Locate every Plasmodium parasite.
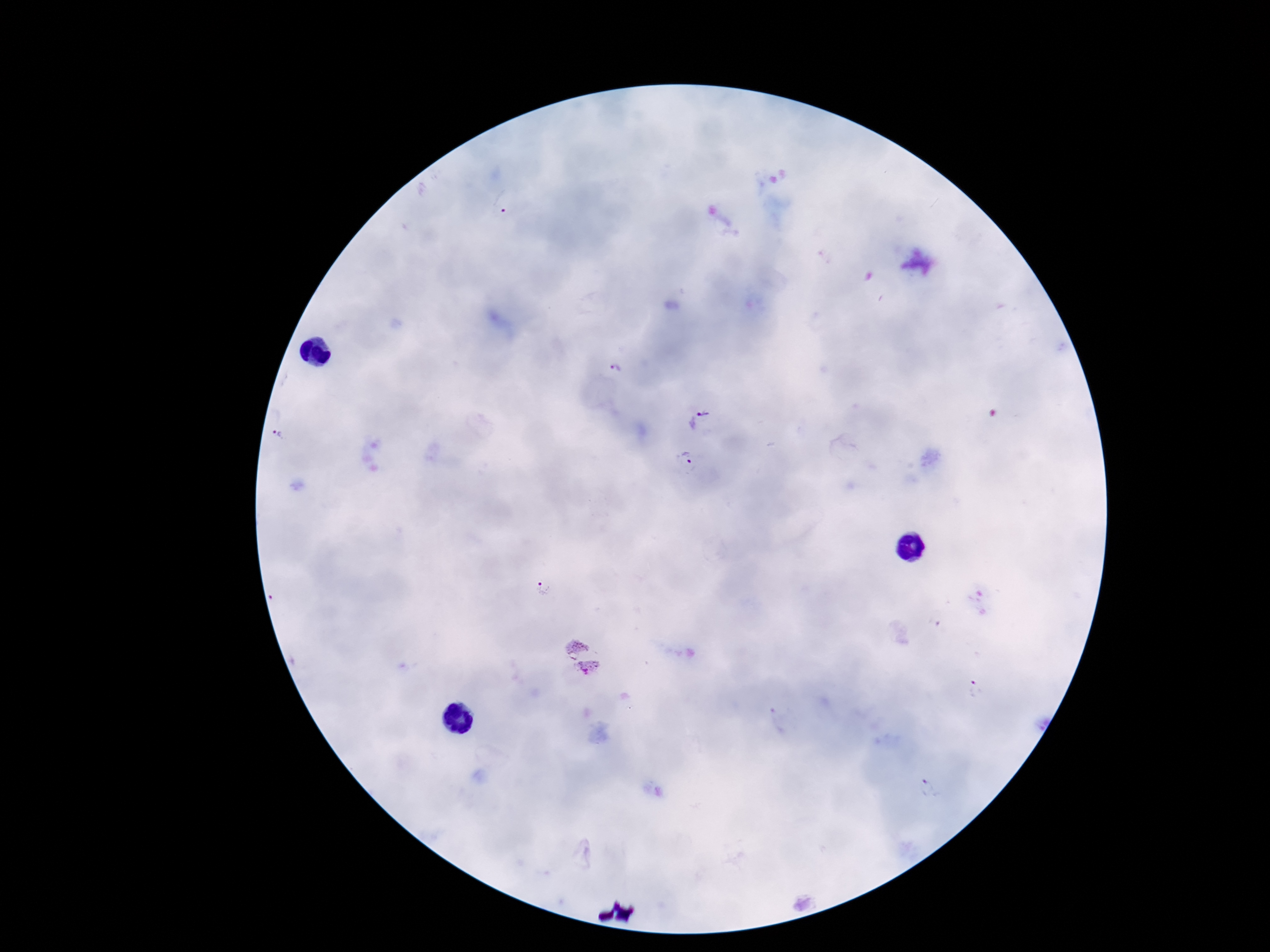

Approximate centers as [x, y] in pixels.
Plasmodium parasites: [505, 202], [615, 375], [704, 423], [284, 436], [684, 463], [539, 589], [974, 689].

field of view = one from this slide
magnification = 100x
stain = Giemsa
capture = smartphone camera through the microscope eyepiece
patient malaria status = infected
image size = 1270×952 pixels
preparation = thick peripheral-blood smear